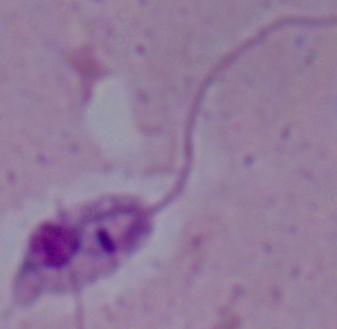
identification = Leishmania
modality = micrograph
magnification = 1000x